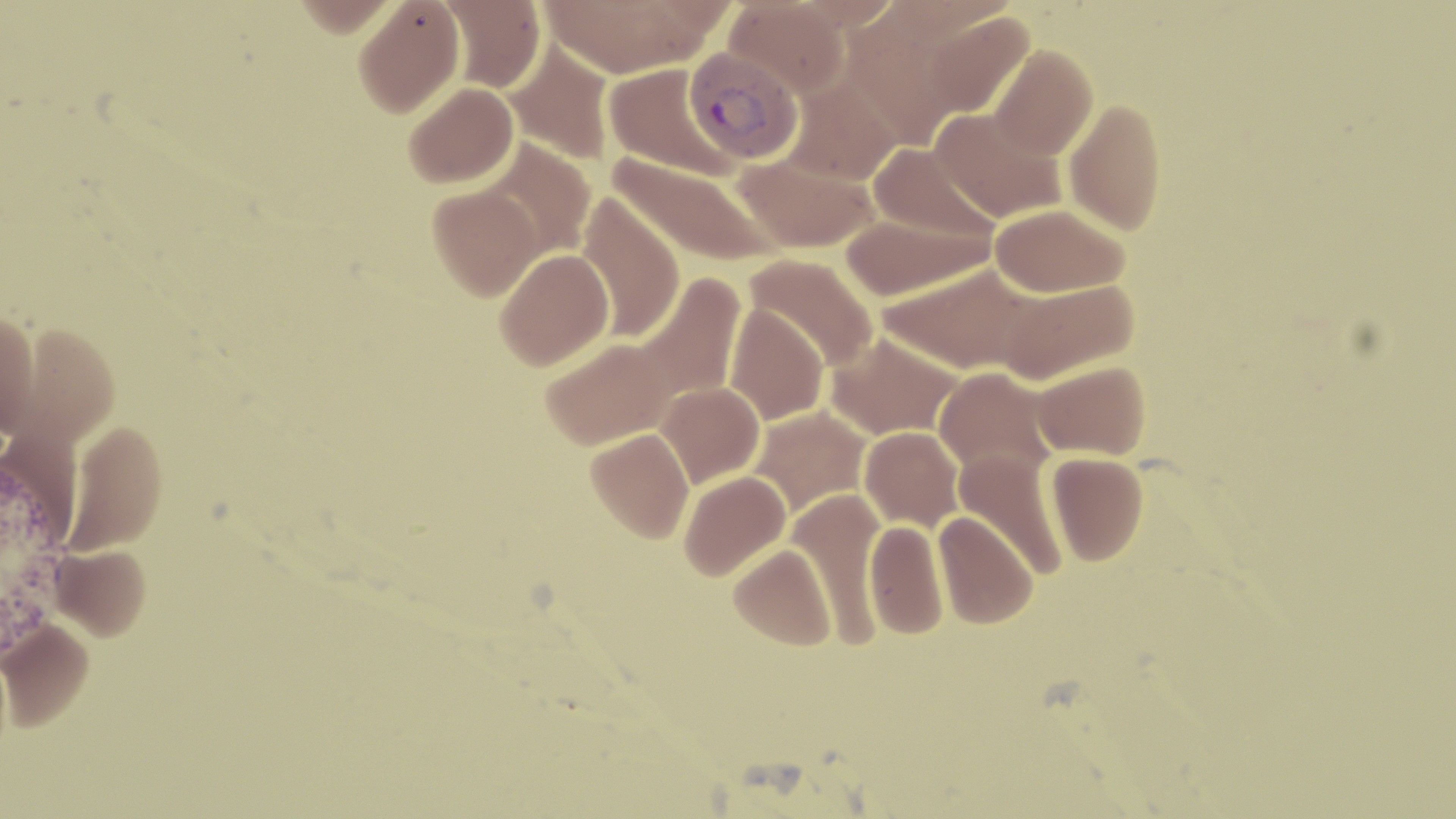 Approximate bounding boxes as (x1,y1)-(x2,y2) corner pairs in pixels. Uninfected red blood cell locations: (292,0)-(402,37), (353,0)-(465,117), (540,0)-(714,77), (723,0)-(850,98), (789,0)-(904,31), (437,1)-(545,92), (922,11)-(1036,123), (502,42)-(617,165), (989,44)-(1098,160), (603,62)-(738,178), (404,81)-(518,188), (1063,97)-(1167,236), (929,106)-(1068,223), (481,139)-(596,259), (867,142)-(998,247), (732,150)-(883,253), (608,153)-(782,268), (428,184)-(544,302), (575,194)-(686,342), (989,203)-(1130,298), (838,212)-(991,302), (494,249)-(614,370), (743,252)-(879,375), (878,263)-(1040,375), (631,273)-(748,406), (996,279)-(1139,385), (725,302)-(829,425), (0,311)-(40,437), (12,323)-(119,448), (825,332)-(964,442), (541,337)-(677,450), (1030,360)-(1150,460), (933,367)-(1058,481), (657,382)-(765,490), (747,405)-(873,520), (64,422)-(168,557), (859,426)-(964,531), (586,428)-(694,542), (953,449)-(1070,578), (1045,451)-(1148,566), (678,470)-(790,580), (788,488)-(888,646), (932,511)-(1038,629), (864,518)-(949,639), (729,542)-(837,650), (50,546)-(151,643), (0,622)-(94,734). Plasmodium vivax-infected red blood cell locations: (682,46)-(804,166). Slide-level diagnosis: Plasmodium vivax. Captured at 1000x magnification. Single field of view. Light microscopy. Thin blood smear. Image is 1456×819 pixels. May-Grünwald-Giemsa stain.